Classify this cell by malaria status.
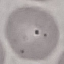
Uninfected.

Photographed with a smartphone camera at the microscope eyepiece. Automatically extracted cell patch, resized to 64 × 64 pixels. Giemsa stain. Thin smear of blood.